Comment on the morphology of the erythrocytes.
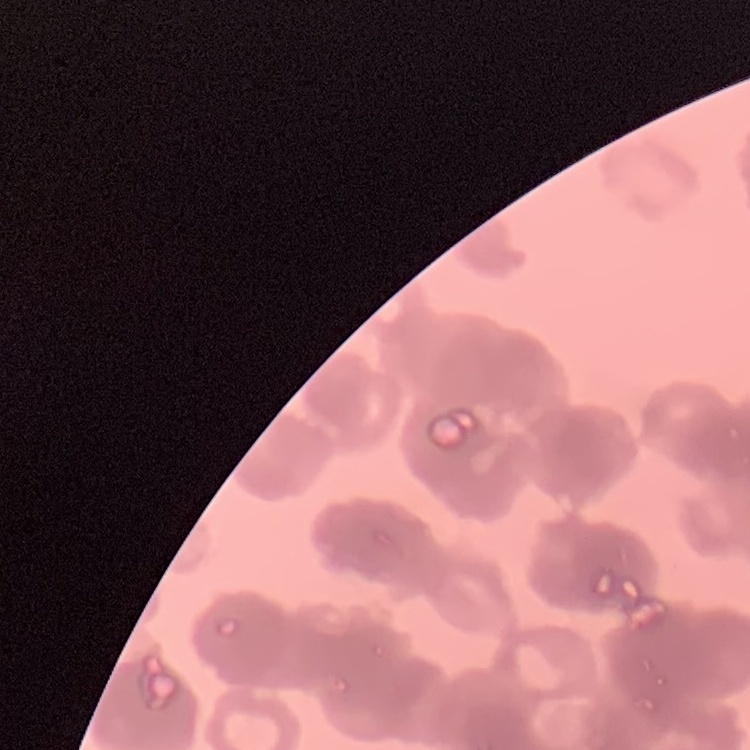
They show rouleaux formation.

Square crop of a larger photomicrograph. Thin blood smear. Field's or Giemsa stain.